Describe the morphology of the red blood cells.
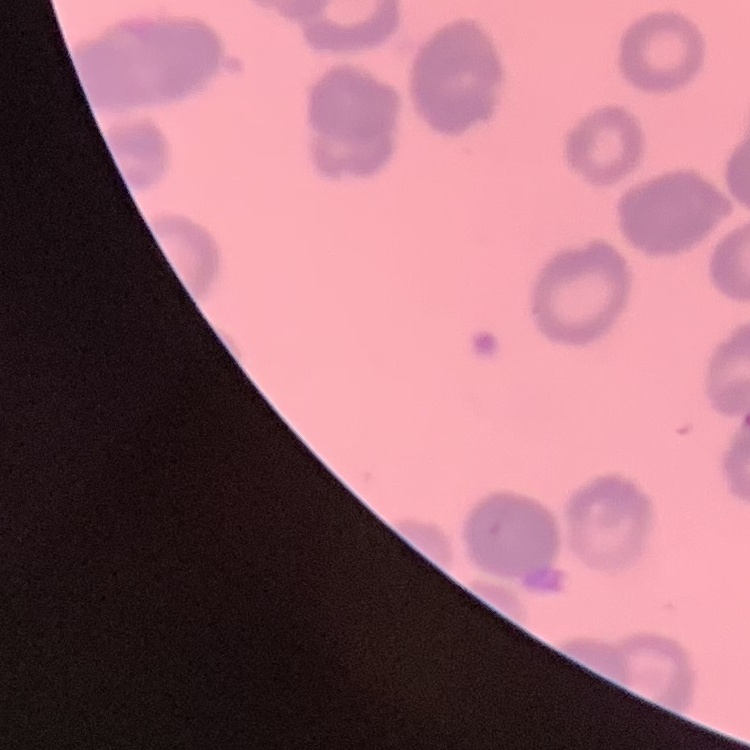
They show rouleaux formation.

{
  "preparation": "thin blood film",
  "stain": "Field's or Giemsa",
  "image_type": "square crop of a larger photomicrograph"
}